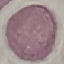
result = no malaria parasites seen
preparation = thin blood film
stain = Giemsa
image type = automatically extracted cell patch, resized to 64 × 64 pixels
capture = smartphone camera at the microscope eyepiece